Report the malaria status of this cell.
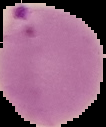

It is parasitized.

preparation = thin blood film
image type = segmented cell region on a black background
image size = 106×127 pixels